Assess this cell for malaria.
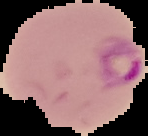

It is parasitized.

Summary:
  - Preparation: thin blood smear
  - Image type: segmented cell region on a black background
  - Image size: 148×136 pixels